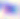
modality = photomicrograph
magnification = 400x
identification = Toxoplasma gondii